Outline each uninfected red blood cell.
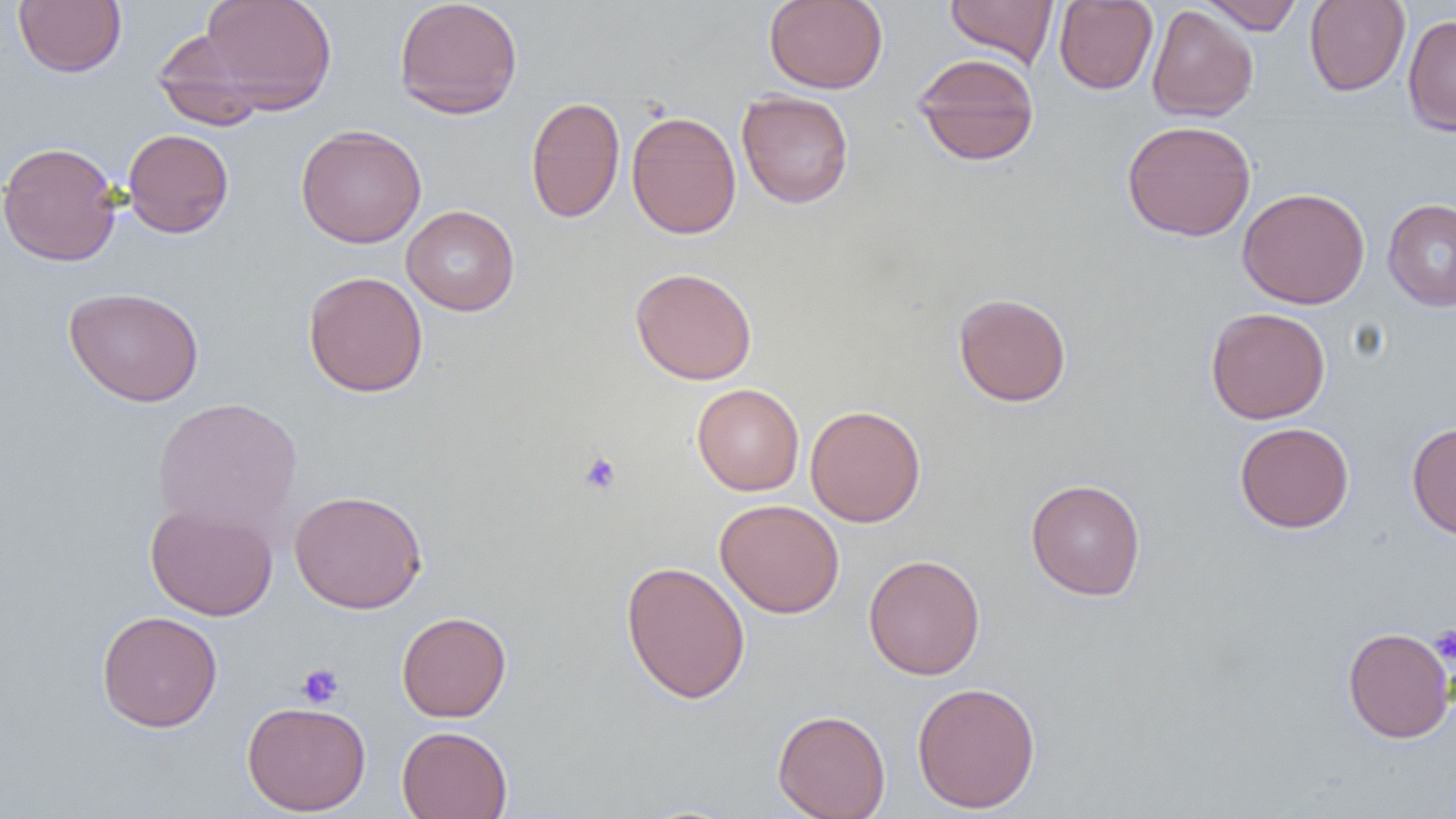
Approximate bounding boxes as (x1,y1)-(x2,y2) corner pairs in pixels.
Uninfected red blood cells: (196,0)-(338,114), (393,0)-(523,119), (764,0)-(888,93), (945,0)-(1059,68), (1198,0)-(1306,34), (1304,0)-(1410,96), (13,1)-(127,77), (1054,1)-(1158,94), (1146,4)-(1259,122), (1402,14)-(1456,136), (151,30)-(272,130), (912,52)-(1040,166), (737,90)-(854,208), (525,96)-(625,223), (625,110)-(741,239), (1121,119)-(1256,241), (295,124)-(427,248), (122,128)-(234,238), (0,141)-(122,267), (1237,187)-(1370,308), (1383,198)-(1456,311), (401,205)-(519,316), (630,267)-(757,385), (303,271)-(429,397), (63,286)-(204,407), (953,292)-(1072,407), (1205,307)-(1331,424), (692,383)-(804,496), (152,397)-(303,537), (805,405)-(926,526), (1234,421)-(1354,534), (1406,421)-(1456,540), (1025,478)-(1146,600), (289,489)-(428,614), (715,499)-(845,618), (145,503)-(278,621), (863,554)-(985,680), (621,560)-(751,704), (96,610)-(223,732), (396,610)-(512,722), (1342,627)-(1455,743), (912,681)-(1041,813), (242,700)-(371,816), (772,709)-(891,819), (396,725)-(513,819).

Platelet locations: (578,450)-(623,496), (1429,623)-(1456,665), (296,663)-(345,707). Slide-level diagnosis: negative for blood parasites. Thin blood smear. Captured at 1000x magnification. Image is 1456×819 pixels. Single field of view. Optical microscopy.